Report the malaria status of this cell.
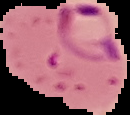

Parasitized.

{
  "preparation": "thin blood smear",
  "image_size": "130×115 pixels",
  "image_type": "segmented cell region with the area outside set to black"
}